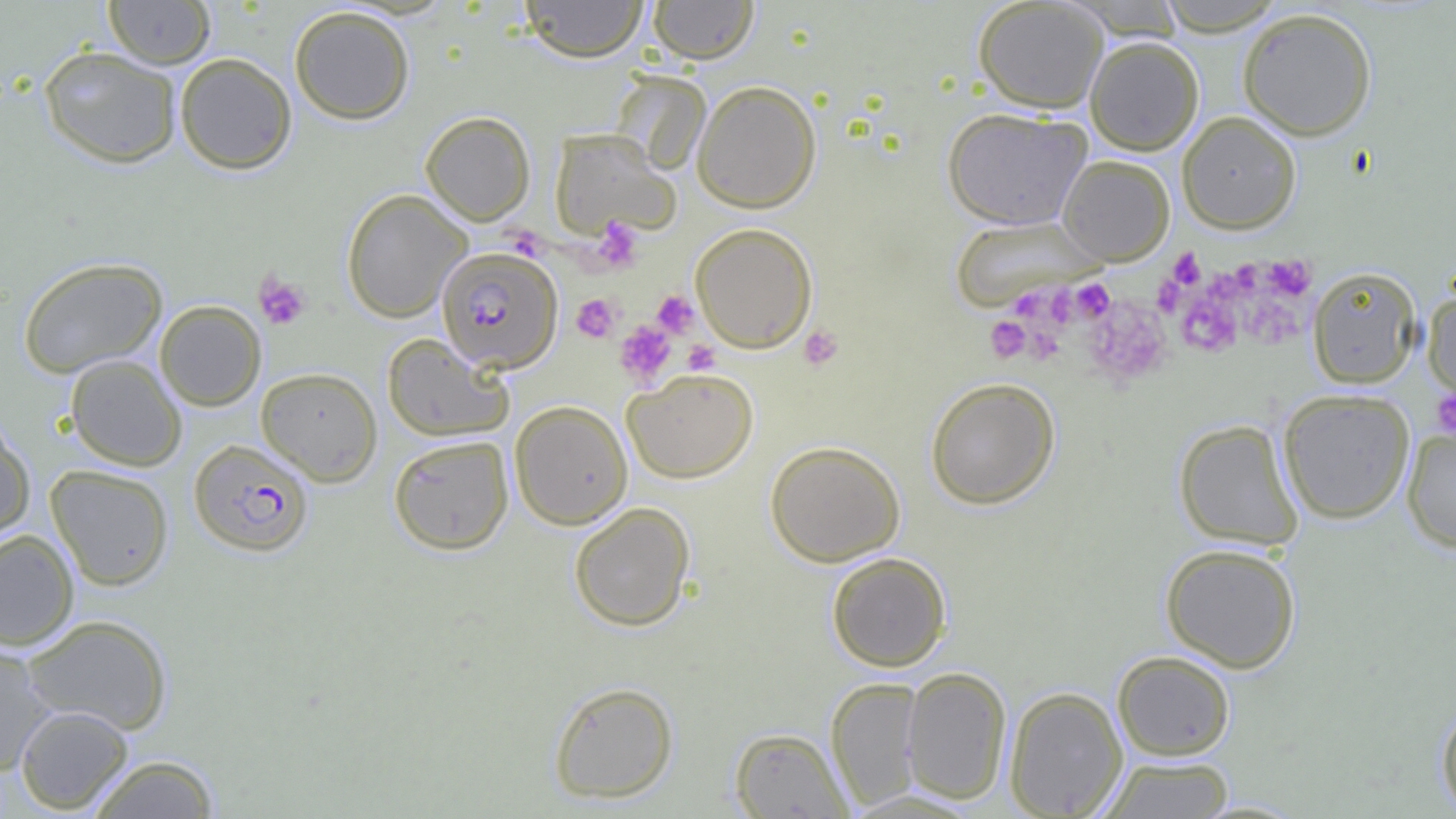

Summary:
  - Coordinate format: approximate bounding boxes as named x1/y1/x2/y2 corners in pixels
  - Plasmodium falciparum-infected red blood cell locations: (x1=436, y1=246, x2=563, y2=373), (x1=189, y1=439, x2=314, y2=556)
  - Uninfected red blood cell locations: (x1=103, y1=0, x2=216, y2=69), (x1=519, y1=0, x2=650, y2=62), (x1=648, y1=0, x2=759, y2=63), (x1=973, y1=0, x2=1108, y2=113), (x1=1154, y1=0, x2=1289, y2=35), (x1=288, y1=5, x2=415, y2=124), (x1=1237, y1=6, x2=1378, y2=141), (x1=1085, y1=36, x2=1204, y2=155), (x1=39, y1=45, x2=182, y2=168), (x1=174, y1=52, x2=297, y2=174), (x1=691, y1=80, x2=822, y2=213), (x1=942, y1=107, x2=1092, y2=230), (x1=419, y1=111, x2=535, y2=225), (x1=1177, y1=112, x2=1301, y2=233), (x1=549, y1=129, x2=680, y2=240), (x1=1057, y1=154, x2=1175, y2=265), (x1=341, y1=189, x2=472, y2=322), (x1=948, y1=217, x2=1104, y2=311), (x1=690, y1=222, x2=818, y2=352), (x1=18, y1=256, x2=168, y2=378), (x1=1306, y1=265, x2=1422, y2=388), (x1=1423, y1=287, x2=1456, y2=403), (x1=154, y1=300, x2=266, y2=411), (x1=381, y1=333, x2=513, y2=442), (x1=65, y1=354, x2=187, y2=471), (x1=256, y1=366, x2=382, y2=486), (x1=623, y1=368, x2=758, y2=483), (x1=924, y1=377, x2=1060, y2=510), (x1=1277, y1=388, x2=1415, y2=524), (x1=509, y1=400, x2=633, y2=529), (x1=0, y1=418, x2=35, y2=545), (x1=1174, y1=418, x2=1304, y2=550), (x1=1402, y1=427, x2=1456, y2=554), (x1=389, y1=435, x2=514, y2=555), (x1=765, y1=440, x2=905, y2=566), (x1=45, y1=464, x2=175, y2=591), (x1=568, y1=502, x2=696, y2=632), (x1=0, y1=529, x2=79, y2=650), (x1=1160, y1=542, x2=1302, y2=673), (x1=826, y1=552, x2=951, y2=671), (x1=21, y1=614, x2=173, y2=735), (x1=0, y1=641, x2=58, y2=776), (x1=1112, y1=650, x2=1236, y2=760), (x1=901, y1=665, x2=1012, y2=804), (x1=825, y1=677, x2=925, y2=810), (x1=548, y1=680, x2=679, y2=804), (x1=1004, y1=686, x2=1128, y2=818), (x1=1435, y1=699, x2=1456, y2=818), (x1=15, y1=705, x2=134, y2=815), (x1=729, y1=727, x2=853, y2=818), (x1=84, y1=754, x2=222, y2=818), (x1=1097, y1=756, x2=1236, y2=818)
  - Platelet locations: (x1=591, y1=219, x2=644, y2=273), (x1=508, y1=228, x2=547, y2=259), (x1=1169, y1=248, x2=1205, y2=289), (x1=1158, y1=252, x2=1198, y2=304), (x1=1263, y1=255, x2=1316, y2=302), (x1=253, y1=272, x2=311, y2=330), (x1=1153, y1=275, x2=1187, y2=317), (x1=1072, y1=279, x2=1114, y2=324), (x1=651, y1=290, x2=700, y2=338), (x1=1241, y1=291, x2=1307, y2=349), (x1=1047, y1=293, x2=1077, y2=328), (x1=1177, y1=293, x2=1241, y2=357), (x1=572, y1=294, x2=620, y2=342), (x1=1015, y1=294, x2=1047, y2=325), (x1=1084, y1=297, x2=1172, y2=387), (x1=985, y1=317, x2=1030, y2=363), (x1=614, y1=320, x2=676, y2=388), (x1=1019, y1=323, x2=1065, y2=365), (x1=798, y1=325, x2=844, y2=371), (x1=683, y1=340, x2=720, y2=375), (x1=1431, y1=387, x2=1456, y2=440)
  - Slide-level diagnosis: Plasmodium falciparum
  - Preparation: thin blood film
  - Modality: light microscopy
  - Field of view: single
  - Magnification: 1000x
  - Image size: 1456×819 pixels